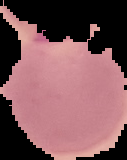 Result: Plasmodium parasites detected. From a thin blood film. Image is 127×160 pixels. Cell region segmented out of the field of view; the surrounding area is masked to black.